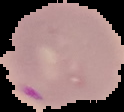
preparation = thin blood smear
image size = 124×112 pixels
image type = segmented cell region on a black background
malaria status = parasitized